Outline each blood parasite and name the species.
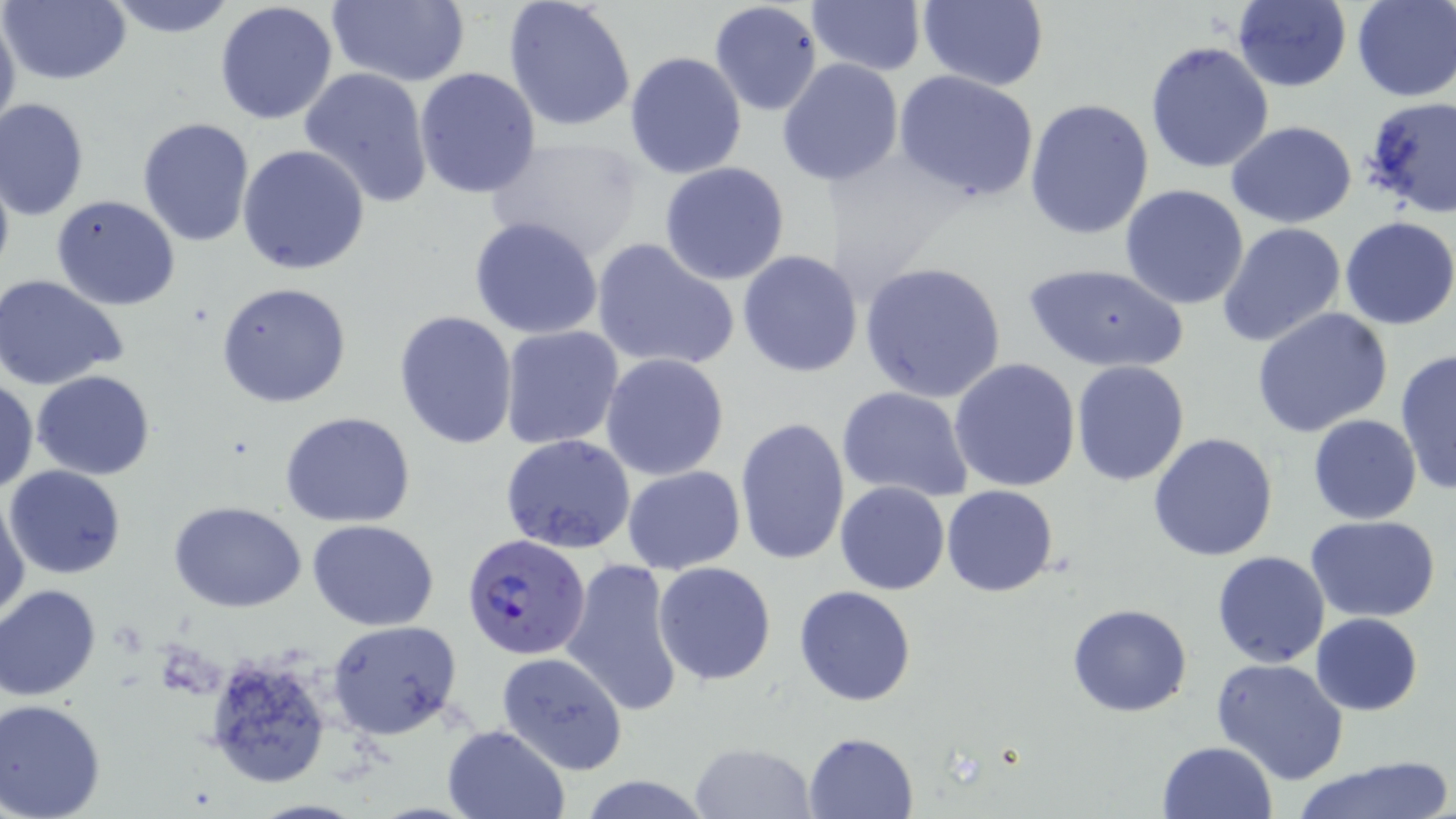
Approximate bounding boxes as (x1, y1, x2, y2) in pixels.
Plasmodium falciparum-infected red blood cells: (465, 534, 594, 662).
No Plasmodium ovale, Plasmodium malariae, Plasmodium vivax, Babesia divergens, or Trypanosoma brucei observed.

slide_level_diagnosis: Plasmodium falciparum
field_of_view: one of a larger specimen
modality: optical microscopy
stain: May-Grünwald-Giemsa
preparation: thin blood smear
uninfected_red_blood_cell_locations: 'approximate bounding boxes as (x1, y1, x2, y2) in pixels: (1, 0, 130, 86), (98, 0, 240, 39), (213, 0, 340, 125), (326, 0, 469, 87), (503, 0, 638, 132), (1351, 0, 1455, 101), (709, 1, 823, 116), (809, 1, 925, 75), (913, 1, 1050, 90), (1229, 1, 1353, 91), (0, 6, 21, 141), (1145, 40, 1274, 175), (624, 51, 747, 179), (777, 58, 904, 187), (299, 66, 435, 207), (414, 68, 542, 198), (894, 70, 1040, 204), (1023, 96, 1154, 239), (0, 99, 89, 221), (1363, 103, 1456, 225), (137, 117, 254, 249), (1227, 120, 1356, 229), (485, 135, 646, 262), (239, 145, 370, 275), (0, 161, 15, 287), (659, 161, 790, 286), (1119, 183, 1251, 310), (50, 193, 182, 310), (468, 215, 605, 339), (1339, 217, 1456, 330), (1218, 223, 1347, 349), (591, 237, 739, 372), (737, 249, 864, 378), (859, 261, 1007, 403), (1021, 262, 1188, 373), (0, 274, 128, 390), (215, 282, 351, 408), (1250, 307, 1393, 437), (394, 309, 519, 450), (499, 325, 624, 450), (1395, 347, 1456, 494), (601, 352, 729, 480), (949, 358, 1081, 491), (1072, 359, 1190, 487), (31, 369, 155, 479), (0, 377, 37, 493), (835, 385, 974, 501), (281, 412, 417, 528), (1307, 414, 1422, 525), (735, 418, 850, 565), (1148, 432, 1279, 560), (501, 433, 635, 554), (6, 465, 126, 580), (624, 466, 745, 574), (835, 481, 950, 596), (942, 485, 1060, 597), (0, 492, 30, 620), (168, 500, 305, 612), (1307, 516, 1442, 621), (308, 519, 440, 631), (1210, 551, 1331, 668), (562, 558, 685, 718), (652, 562, 776, 685), (0, 583, 102, 701), (795, 585, 917, 707), (1066, 604, 1193, 717), (1310, 613, 1423, 715), (327, 619, 463, 739), (201, 648, 334, 790), (496, 651, 628, 775), (1211, 658, 1351, 786), (0, 699, 106, 819), (441, 724, 568, 819), (803, 731, 917, 817), (1157, 741, 1277, 819), (690, 742, 814, 818), (1292, 758, 1451, 819), (577, 777, 715, 818)'
image_size: 1456×819 pixels
magnification: 1000x